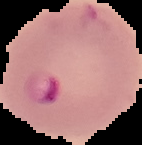

image type = cell region segmented out of the field of view; surrounding area masked to black
image size = 142×145 pixels
malaria status = parasitized
preparation = thin blood smear